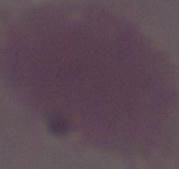 1000x magnification. Micrograph. An erythrocyte is shown.